Assess this cell for malaria.
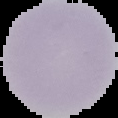
It is uninfected.

Summary:
  - Image size: 118×118 pixels
  - Image type: segmented cell region with the area outside set to black
  - Preparation: thin blood smear